Report the malaria status of this cell.
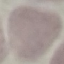
Uninfected.

Acquired by smartphone through the microscope eyepiece. Giemsa-stained preparation. Automatically extracted cell patch, resized to 64 × 64 pixels. Thin blood smear.